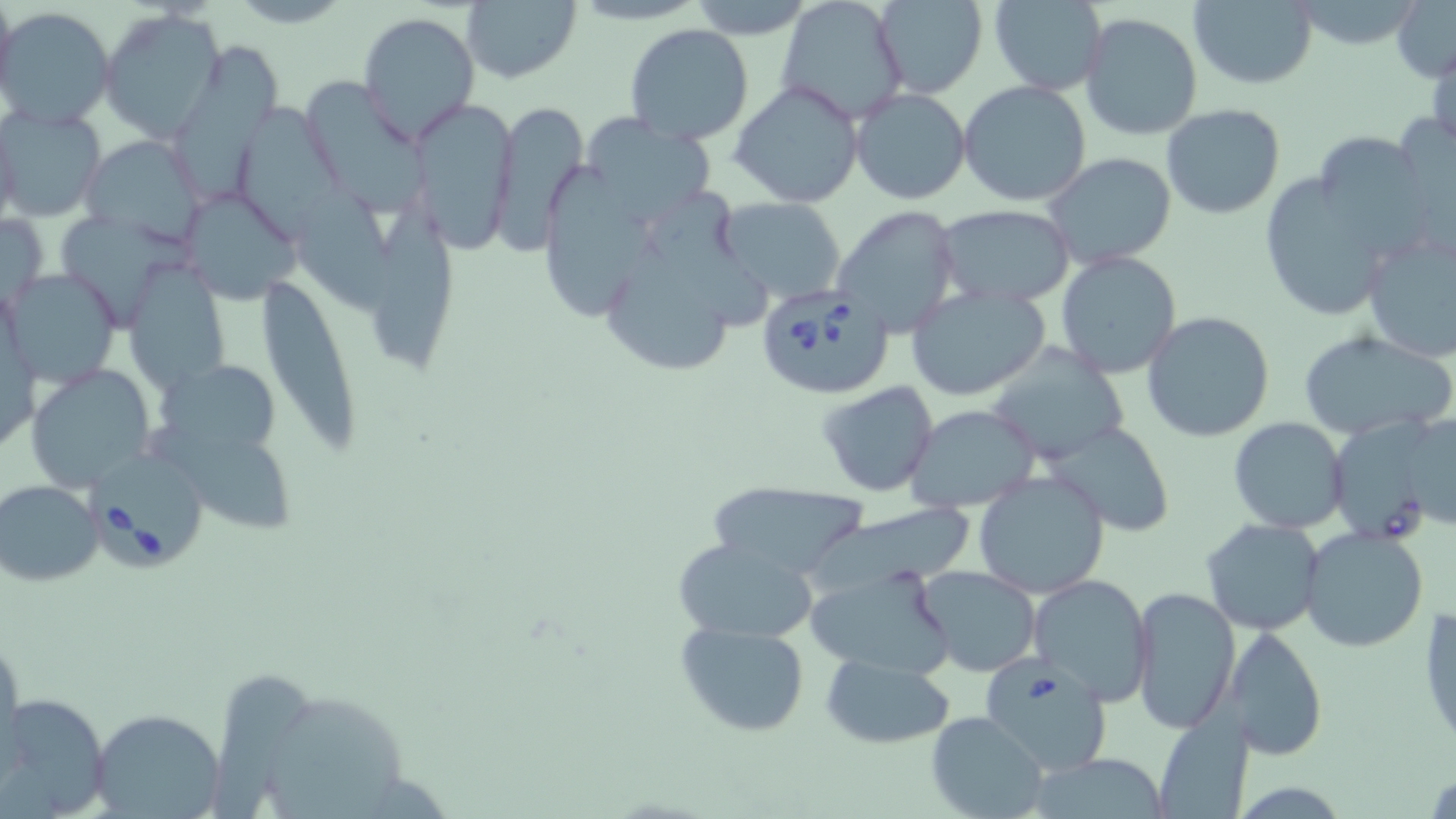

slide-level diagnosis = Babesia divergens
uninfected red blood cell locations = approximate bounding boxes as named x1/y1/x2/y2 corners in pixels: (x1=0, y1=0, x2=19, y2=110), (x1=776, y1=0, x2=911, y2=124), (x1=870, y1=0, x2=987, y2=100), (x1=988, y1=0, x2=1107, y2=95), (x1=461, y1=1, x2=582, y2=84), (x1=681, y1=1, x2=820, y2=36), (x1=1189, y1=1, x2=1319, y2=89), (x1=1391, y1=2, x2=1456, y2=82), (x1=99, y1=7, x2=228, y2=142), (x1=0, y1=8, x2=116, y2=128), (x1=356, y1=12, x2=478, y2=147), (x1=1079, y1=12, x2=1203, y2=141), (x1=623, y1=24, x2=754, y2=146), (x1=176, y1=34, x2=285, y2=203), (x1=1428, y1=34, x2=1456, y2=152), (x1=309, y1=69, x2=431, y2=219), (x1=729, y1=79, x2=866, y2=209), (x1=957, y1=81, x2=1092, y2=207), (x1=850, y1=87, x2=972, y2=205), (x1=407, y1=98, x2=515, y2=250), (x1=487, y1=99, x2=590, y2=255), (x1=240, y1=102, x2=353, y2=236), (x1=1161, y1=105, x2=1287, y2=219), (x1=0, y1=106, x2=105, y2=224), (x1=0, y1=110, x2=21, y2=236), (x1=578, y1=114, x2=717, y2=227), (x1=1311, y1=128, x2=1430, y2=253), (x1=82, y1=135, x2=204, y2=243), (x1=1045, y1=151, x2=1177, y2=269), (x1=536, y1=159, x2=643, y2=318), (x1=1256, y1=168, x2=1394, y2=318), (x1=296, y1=185, x2=390, y2=323), (x1=648, y1=190, x2=767, y2=327), (x1=180, y1=193, x2=304, y2=306), (x1=717, y1=197, x2=849, y2=306), (x1=832, y1=203, x2=961, y2=337), (x1=935, y1=204, x2=1076, y2=307), (x1=366, y1=205, x2=462, y2=372), (x1=62, y1=208, x2=189, y2=319), (x1=1, y1=211, x2=48, y2=310), (x1=1360, y1=228, x2=1456, y2=365), (x1=617, y1=237, x2=743, y2=373), (x1=1054, y1=251, x2=1182, y2=379), (x1=126, y1=267, x2=231, y2=401), (x1=5, y1=270, x2=121, y2=389), (x1=256, y1=271, x2=366, y2=455), (x1=906, y1=286, x2=1050, y2=400), (x1=1141, y1=311, x2=1277, y2=444), (x1=1298, y1=329, x2=1454, y2=439), (x1=982, y1=340, x2=1131, y2=466), (x1=25, y1=364, x2=153, y2=491), (x1=159, y1=365, x2=284, y2=452), (x1=817, y1=381, x2=940, y2=498), (x1=905, y1=403, x2=1040, y2=511), (x1=1229, y1=417, x2=1349, y2=533), (x1=1048, y1=422, x2=1173, y2=537), (x1=1334, y1=424, x2=1432, y2=550), (x1=148, y1=430, x2=295, y2=532), (x1=974, y1=471, x2=1109, y2=598), (x1=1, y1=478, x2=105, y2=586), (x1=701, y1=482, x2=872, y2=579), (x1=790, y1=489, x2=978, y2=595), (x1=1200, y1=518, x2=1327, y2=637), (x1=1293, y1=528, x2=1423, y2=655), (x1=672, y1=538, x2=820, y2=643), (x1=805, y1=563, x2=957, y2=678), (x1=913, y1=565, x2=1043, y2=677), (x1=1027, y1=576, x2=1153, y2=705), (x1=1130, y1=585, x2=1240, y2=735), (x1=1418, y1=604, x2=1456, y2=752), (x1=675, y1=619, x2=812, y2=738), (x1=1233, y1=627, x2=1328, y2=760), (x1=821, y1=652, x2=955, y2=748), (x1=209, y1=672, x2=321, y2=818), (x1=12, y1=694, x2=108, y2=812), (x1=274, y1=697, x2=404, y2=816), (x1=89, y1=708, x2=226, y2=817), (x1=926, y1=711, x2=1050, y2=819), (x1=1154, y1=711, x2=1252, y2=819), (x1=1024, y1=754, x2=1178, y2=817)
preparation = thin blood smear
Babesia divergens-infected red blood cell locations = approximate bounding boxes as named x1/y1/x2/y2 corners in pixels: (x1=756, y1=284, x2=894, y2=400), (x1=89, y1=452, x2=210, y2=572), (x1=978, y1=651, x2=1114, y2=778)
stain = May-Grünwald-Giemsa
image size = 1456×819 pixels
modality = light microscopy
field of view = single
magnification = 1000x